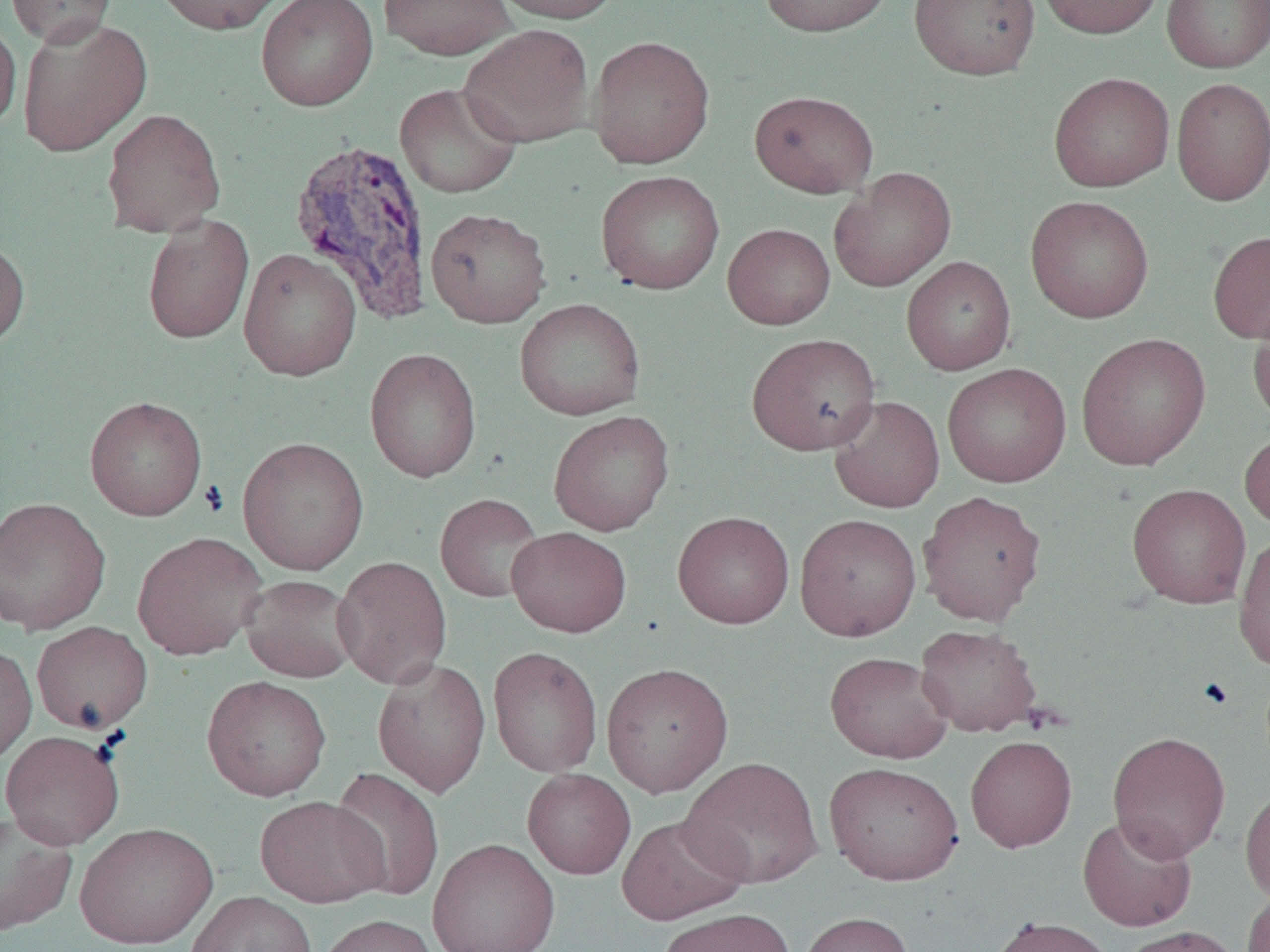 Approximate bounding boxes as [x1, y1, x2, y2] in pixels. Uninfected red blood cell locations: [4, 0, 117, 47], [151, 0, 286, 35], [256, 0, 378, 111], [377, 0, 516, 61], [489, 0, 623, 24], [759, 0, 892, 37], [908, 0, 1040, 81], [1036, 0, 1164, 39], [1162, 0, 1269, 73], [0, 16, 21, 134], [17, 16, 153, 157], [459, 24, 594, 148], [588, 35, 714, 169], [1048, 72, 1174, 192], [1171, 77, 1270, 206], [394, 82, 523, 199], [749, 90, 878, 198], [101, 108, 226, 239], [828, 166, 956, 292], [596, 170, 725, 294], [1025, 195, 1154, 323], [425, 207, 551, 328], [142, 215, 254, 344], [723, 223, 835, 330], [1207, 230, 1270, 344], [0, 236, 30, 351], [238, 247, 362, 381], [901, 256, 1016, 376], [514, 298, 646, 420], [1248, 302, 1270, 425], [1076, 332, 1211, 470], [746, 333, 881, 456], [364, 348, 482, 483], [941, 362, 1071, 488], [828, 395, 945, 513], [84, 396, 207, 521], [548, 410, 675, 536], [1239, 427, 1270, 531], [237, 436, 369, 575], [1127, 483, 1251, 608], [916, 490, 1047, 626], [435, 493, 545, 603], [0, 496, 111, 636], [672, 511, 795, 629], [794, 513, 921, 641], [506, 526, 632, 637], [132, 531, 267, 660], [1233, 531, 1270, 671], [332, 556, 453, 689], [240, 574, 360, 682], [31, 621, 153, 734], [915, 623, 1041, 736], [0, 643, 37, 766], [487, 646, 603, 778], [825, 651, 953, 763], [372, 658, 491, 798], [601, 661, 733, 797], [201, 675, 331, 801], [0, 730, 125, 850], [1107, 731, 1231, 861], [965, 735, 1077, 852], [680, 756, 823, 889], [823, 761, 964, 886], [328, 768, 445, 902], [522, 768, 635, 879], [1240, 785, 1270, 905], [255, 795, 388, 908], [0, 812, 78, 937], [617, 814, 749, 926], [1077, 814, 1197, 932], [75, 821, 218, 949], [427, 837, 560, 952], [1242, 887, 1270, 952], [185, 890, 317, 952], [656, 907, 796, 952], [798, 911, 914, 952], [315, 914, 439, 952], [988, 916, 1119, 952], [1118, 926, 1243, 952]. Plasmodium vivax-infected red blood cell locations: [288, 138, 434, 323]. Slide-level diagnosis: Plasmodium vivax. Optical microscopy. 1000x magnification. Image is 1270×952 pixels. One field of a larger specimen. Thin blood smear.